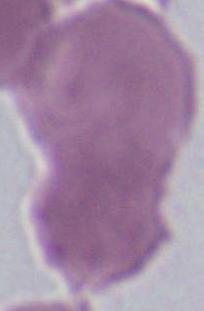

Photomicrograph. An erythrocyte is seen. 1000x magnification.